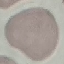
Summary:
  - Result: negative for malaria parasites
  - Image type: cell patch, automatically extracted from a larger field of view and resized to 64 × 64 pixels
  - Preparation: thin smear
  - Capture: smartphone through the microscope eyepiece
  - Stain: Giemsa